Report the malaria status of this cell.
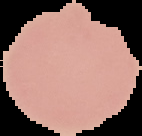

Uninfected.

Summary:
  - Image size: 142×136 pixels
  - Image type: segmented cell region with the area outside set to black
  - Preparation: thin blood smear